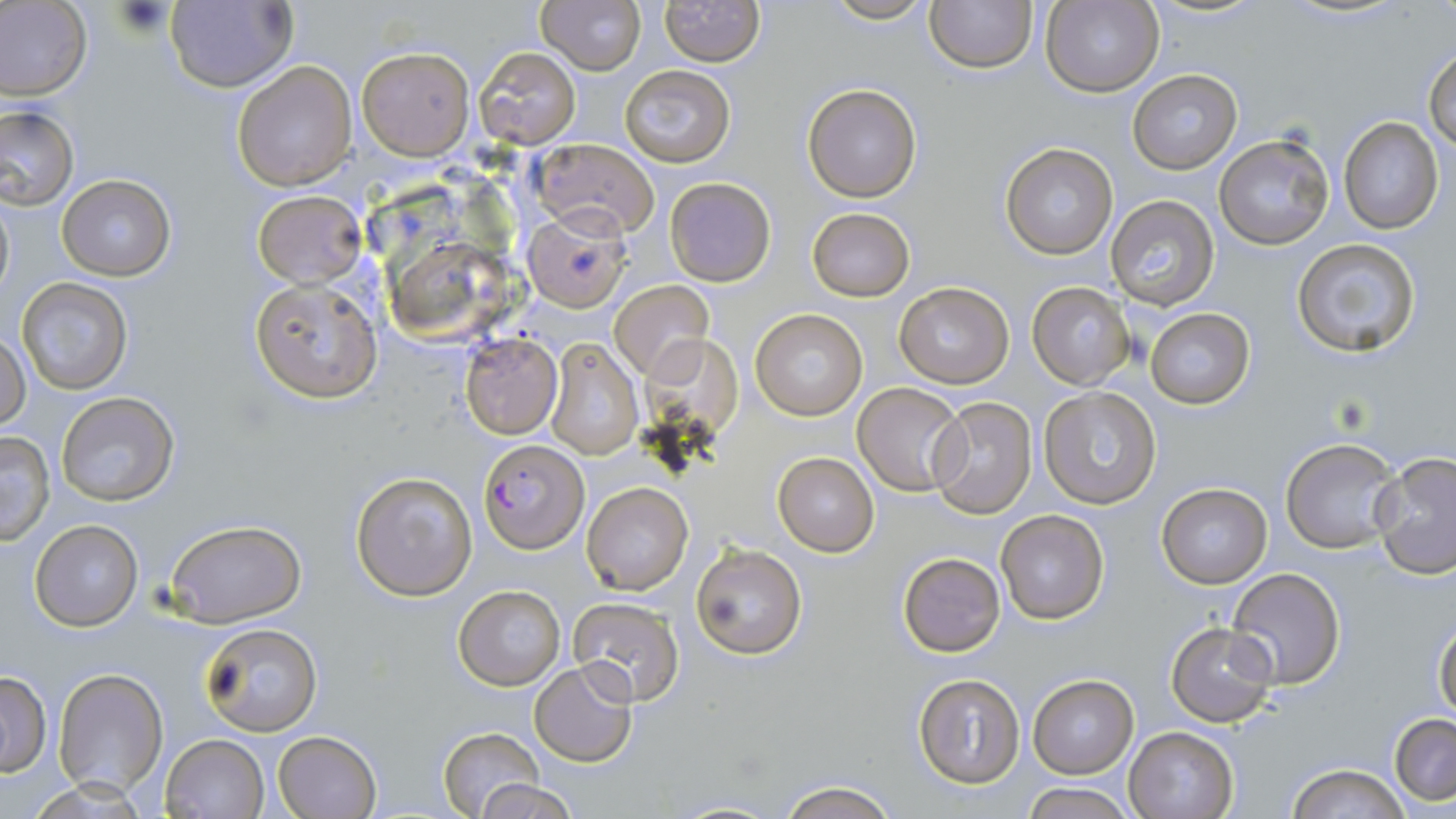

Summary:
  - Coordinate format: approximate bounding boxes as named x1/y1/x2/y2 corners in pixels
  - Plasmodium falciparum-infected red blood cell locations: (x1=480, y1=439, x2=588, y2=554)
  - Uninfected red blood cell locations: (x1=0, y1=0, x2=92, y2=102), (x1=540, y1=0, x2=646, y2=75), (x1=661, y1=0, x2=763, y2=66), (x1=821, y1=0, x2=938, y2=25), (x1=163, y1=1, x2=296, y2=92), (x1=925, y1=1, x2=1037, y2=73), (x1=1041, y1=1, x2=1164, y2=98), (x1=1424, y1=45, x2=1456, y2=153), (x1=357, y1=46, x2=473, y2=158), (x1=475, y1=47, x2=580, y2=148), (x1=231, y1=60, x2=358, y2=190), (x1=620, y1=66, x2=735, y2=166), (x1=1128, y1=69, x2=1242, y2=173), (x1=803, y1=84, x2=921, y2=202), (x1=0, y1=106, x2=79, y2=210), (x1=1337, y1=118, x2=1444, y2=235), (x1=1213, y1=132, x2=1335, y2=248), (x1=532, y1=138, x2=660, y2=238), (x1=1000, y1=142, x2=1117, y2=259), (x1=57, y1=174, x2=176, y2=281), (x1=664, y1=177, x2=775, y2=286), (x1=0, y1=189, x2=14, y2=304), (x1=254, y1=189, x2=365, y2=287), (x1=1107, y1=194, x2=1220, y2=312), (x1=523, y1=208, x2=631, y2=311), (x1=807, y1=208, x2=914, y2=301), (x1=1290, y1=237, x2=1422, y2=357), (x1=389, y1=238, x2=508, y2=347), (x1=18, y1=278, x2=134, y2=395), (x1=250, y1=278, x2=383, y2=402), (x1=610, y1=280, x2=714, y2=382), (x1=893, y1=282, x2=1015, y2=387), (x1=1027, y1=282, x2=1132, y2=389), (x1=1145, y1=308, x2=1254, y2=409), (x1=750, y1=309, x2=867, y2=421), (x1=1, y1=332, x2=29, y2=430), (x1=459, y1=332, x2=563, y2=439), (x1=543, y1=337, x2=644, y2=458), (x1=853, y1=382, x2=969, y2=497), (x1=1037, y1=386, x2=1163, y2=510), (x1=57, y1=392, x2=180, y2=507), (x1=928, y1=396, x2=1038, y2=519), (x1=0, y1=432, x2=57, y2=545), (x1=1280, y1=436, x2=1404, y2=555), (x1=773, y1=452, x2=880, y2=556), (x1=1371, y1=453, x2=1456, y2=578), (x1=351, y1=471, x2=477, y2=600), (x1=1154, y1=482, x2=1273, y2=588), (x1=582, y1=483, x2=693, y2=594), (x1=995, y1=509, x2=1109, y2=624), (x1=166, y1=519, x2=306, y2=627), (x1=30, y1=520, x2=142, y2=631), (x1=693, y1=543, x2=807, y2=660), (x1=897, y1=552, x2=1006, y2=657), (x1=1226, y1=567, x2=1346, y2=688), (x1=454, y1=584, x2=564, y2=692), (x1=567, y1=597, x2=685, y2=706), (x1=1432, y1=616, x2=1455, y2=722), (x1=198, y1=622, x2=323, y2=737), (x1=1166, y1=622, x2=1279, y2=729), (x1=529, y1=661, x2=639, y2=768), (x1=53, y1=669, x2=168, y2=796), (x1=0, y1=671, x2=52, y2=776), (x1=912, y1=673, x2=1027, y2=787), (x1=1026, y1=673, x2=1140, y2=778), (x1=1389, y1=714, x2=1456, y2=806), (x1=1124, y1=727, x2=1238, y2=818), (x1=438, y1=728, x2=545, y2=816), (x1=274, y1=730, x2=381, y2=818), (x1=160, y1=734, x2=268, y2=818), (x1=1287, y1=765, x2=1411, y2=819), (x1=470, y1=778, x2=582, y2=818), (x1=1021, y1=780, x2=1134, y2=818), (x1=775, y1=781, x2=900, y2=819), (x1=664, y1=799, x2=783, y2=818)
  - Slide-level diagnosis: Plasmodium falciparum
  - Magnification: 1000x
  - Image size: 1456×819 pixels
  - Preparation: thin blood smear
  - Field of view: single
  - Modality: light microscopy
  - Stain: May-Grünwald-Giemsa